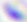

Summary:
  - Identification: Toxoplasma gondii
  - Magnification: 400x
  - Modality: micrograph